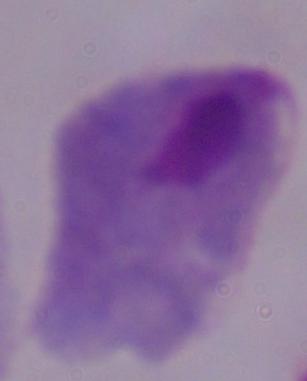 Photomicrograph. Captured at 1000x magnification. A trichomonad is shown.